Locate every Plasmodium ovale-infected red blood cell.
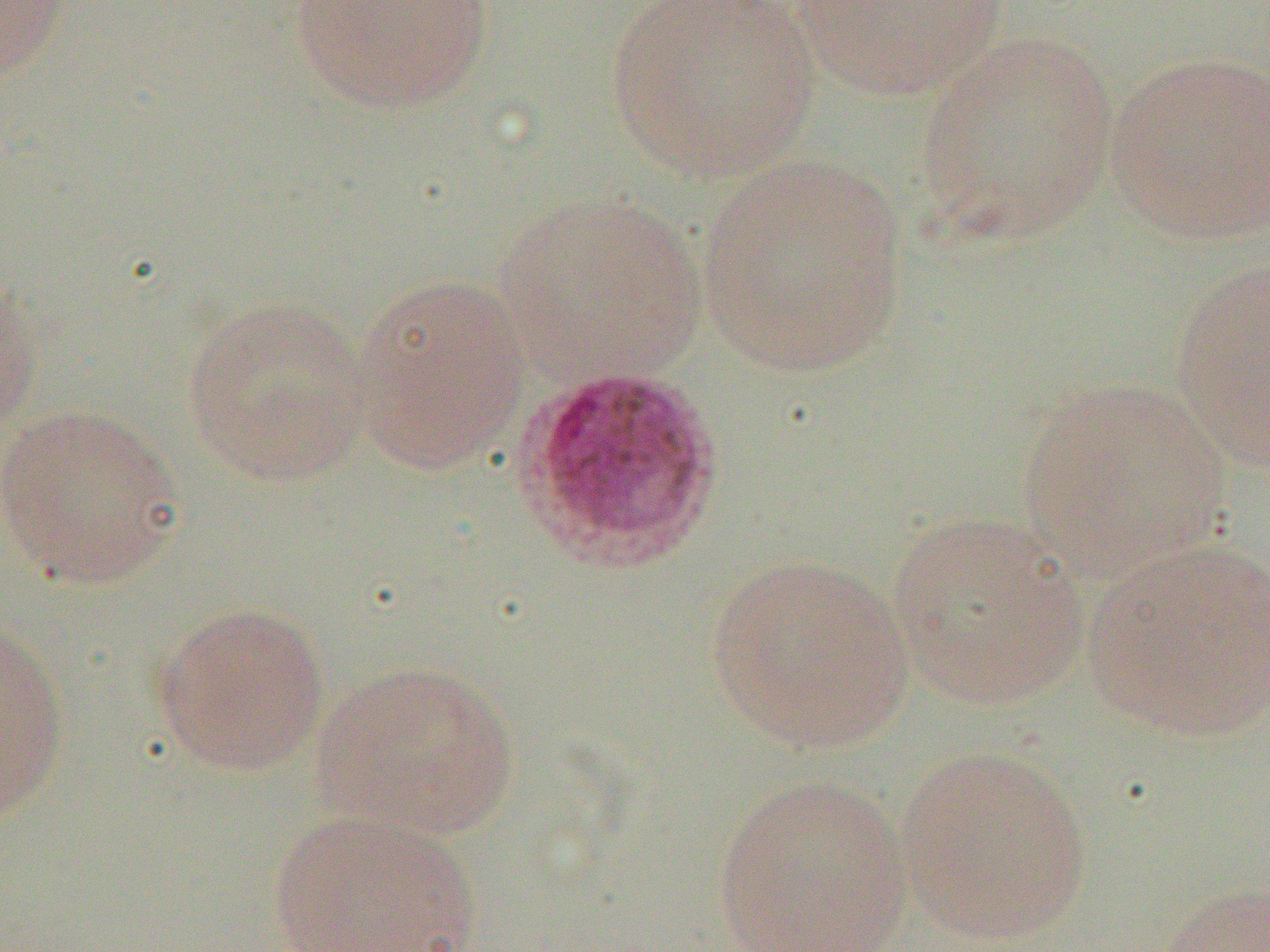

Approximate bounding boxes as [x1, y1, x2, y2] in pixels.
Plasmodium ovale-infected red blood cells: [513, 363, 724, 571].

{
  "slide_level_diagnosis": "Plasmodium ovale",
  "magnification": "1000x",
  "uninfected_red_blood_cell_locations": "approximate bounding boxes as [x1, y1, x2, y2] in pixels: [0, 0, 71, 80], [287, 0, 496, 116], [604, 0, 824, 184], [787, 1, 1010, 100], [914, 31, 1121, 248], [1104, 51, 1270, 246], [696, 156, 910, 377], [495, 190, 708, 382], [1169, 259, 1270, 473], [0, 266, 41, 441], [348, 273, 534, 478], [181, 296, 375, 487], [1016, 376, 1235, 580], [0, 402, 187, 591], [887, 510, 1091, 712], [1082, 538, 1268, 743], [706, 553, 916, 755], [152, 601, 331, 777], [0, 622, 70, 825], [313, 658, 524, 840], [894, 745, 1095, 948], [713, 773, 914, 951], [265, 807, 486, 952], [1157, 882, 1270, 952]",
  "preparation": "thin blood film",
  "field_of_view": "single",
  "image_size": "1270×952 pixels",
  "modality": "light microscopy"
}